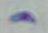
Micrograph. Captured at 1000x magnification. Toxoplasma gondii is shown.